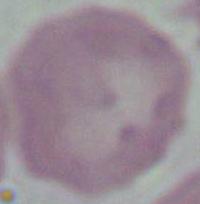 Micrograph. An erythrocyte is shown. Captured at 1000x magnification.